Locate every leukocyte (white blood cell).
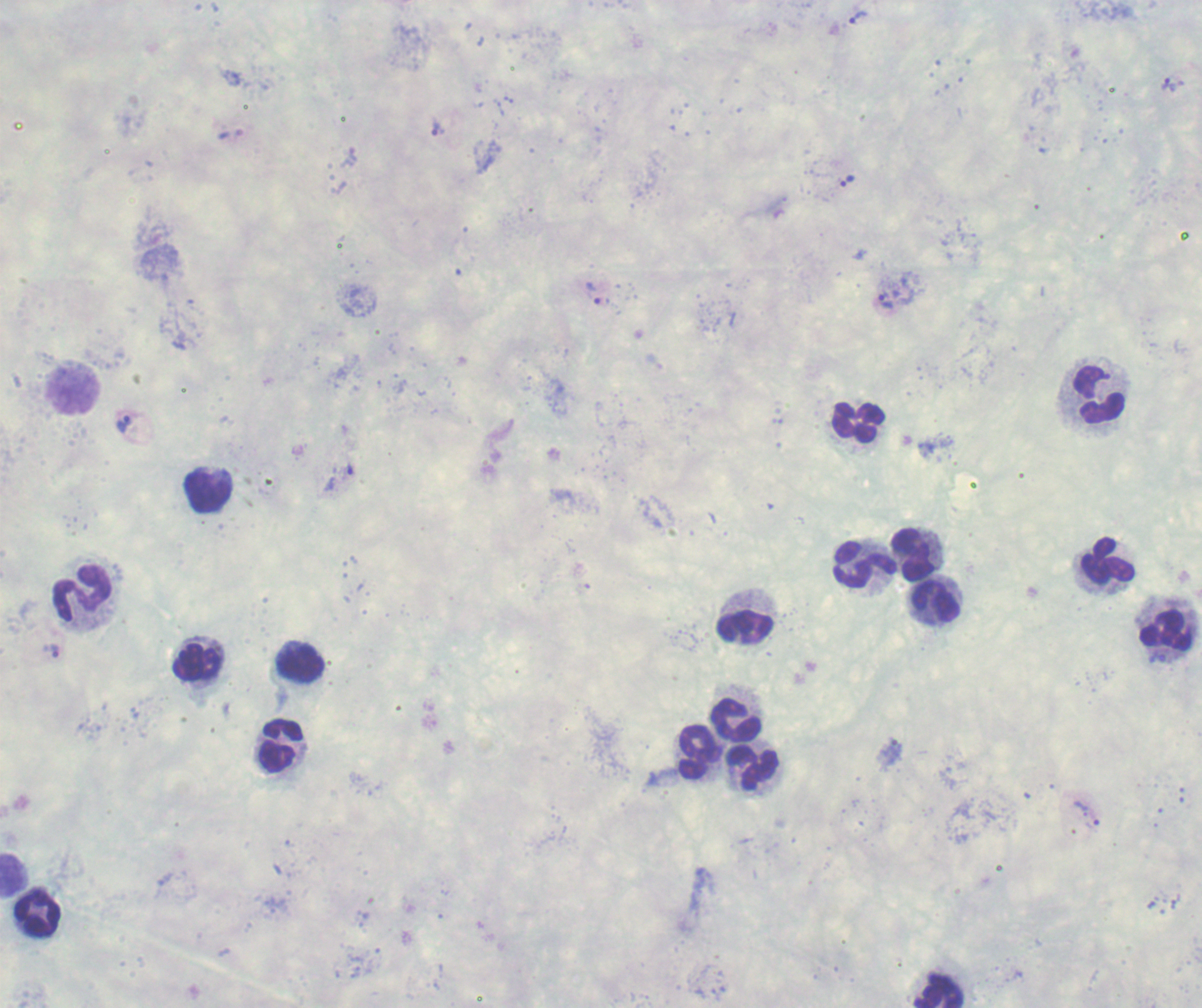

Approximate centers as [x, y] in pixels.
Leukocytes: [1100, 396], [857, 421], [209, 491], [917, 554], [1109, 561], [865, 564], [83, 595], [935, 603], [747, 620], [1166, 627], [299, 661], [198, 662], [735, 720], [281, 746], [698, 754], [752, 768], [15, 873], [37, 913], [938, 990].

Approximate centers as [x, y] in pixels. Trophozoite locations: [858, 17], [1172, 84], [438, 128], [847, 181], [593, 293], [886, 302], [124, 423], [348, 469], [51, 651], [1157, 658], [890, 753], [1086, 815], [1175, 902]. Thick blood film. Image is 1202×1008 pixels. Result: malaria parasites detected. Romanowsky-stained preparation. One field from this slide. Background quality: poor. Previously used in an actual diagnosis. 100x magnification.